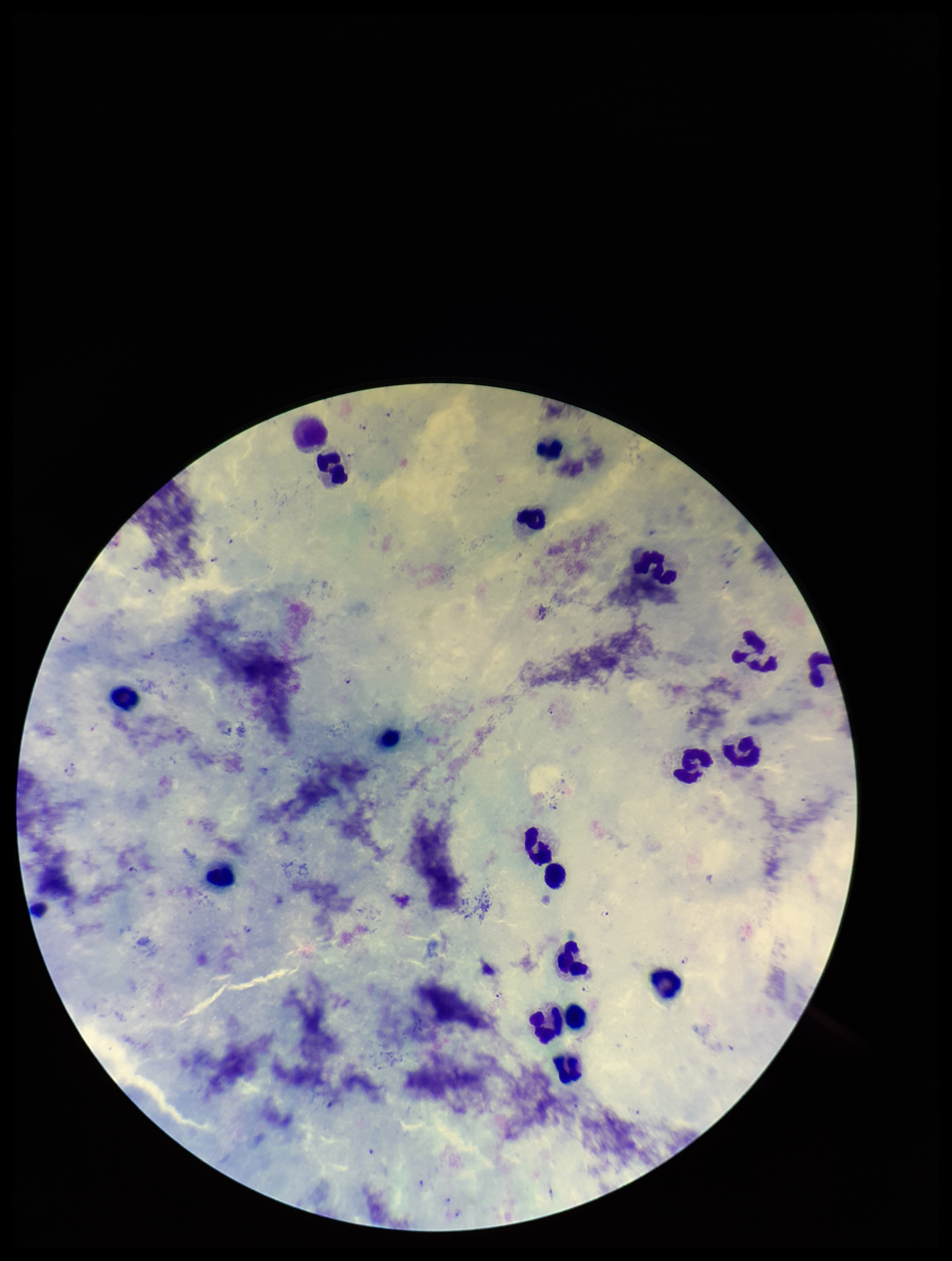
Single field of view. Parasite count: 13. Leukocyte count: 19. Image is 952×1261 pixels. Photographed through the microscope eyepiece with a smartphone camera. Plasmodium parasites: seen. Stained with Giemsa. Patient malaria status: infected. Species reported for this patient: Plasmodium falciparum. Preparation: thick.